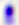
modality = micrograph
magnification = 400x
identification = Toxoplasma gondii